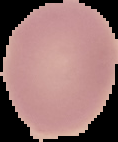 Image is 118×142 pixels. Result: negative for Plasmodium parasites. From a thin blood smear. Cell region segmented out of the field of view; the surrounding area is masked to black.